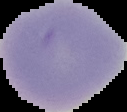
result: no malaria parasites detected
image_size: 127×112 pixels
preparation: thin blood film
image_type: cell region segmented out of the field of view; surrounding area masked to black